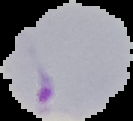
preparation: thin blood smear
image_type: cell region segmented out of the field of view; surrounding area masked to black
image_size: 133×121 pixels
malaria_status: parasitized